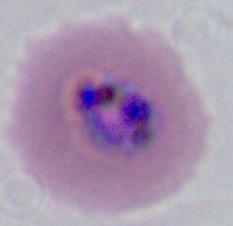
magnification = 400x or 1000x
identification = Plasmodium
modality = photomicrograph